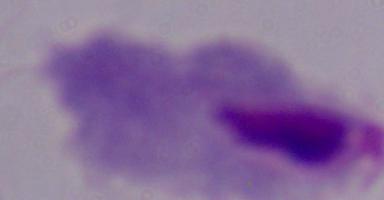
Micrograph. Captured at 1000x magnification. A trichomonad is seen.